Classify this cell by malaria status.
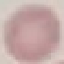

Uninfected.

Summary:
  - Capture: smartphone through the microscope eyepiece
  - Stain: Giemsa
  - Preparation: thin smear
  - Image type: automatically extracted cell patch, resized to 64 × 64 pixels